State which parasite is depicted.
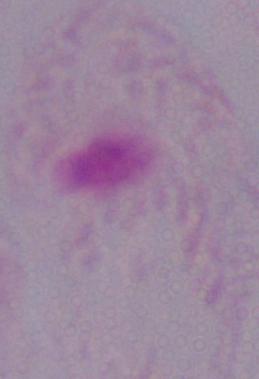

A trichomonad.

Captured at 1000x magnification. Photomicrograph.